Assess the morphology of the erythrocytes.
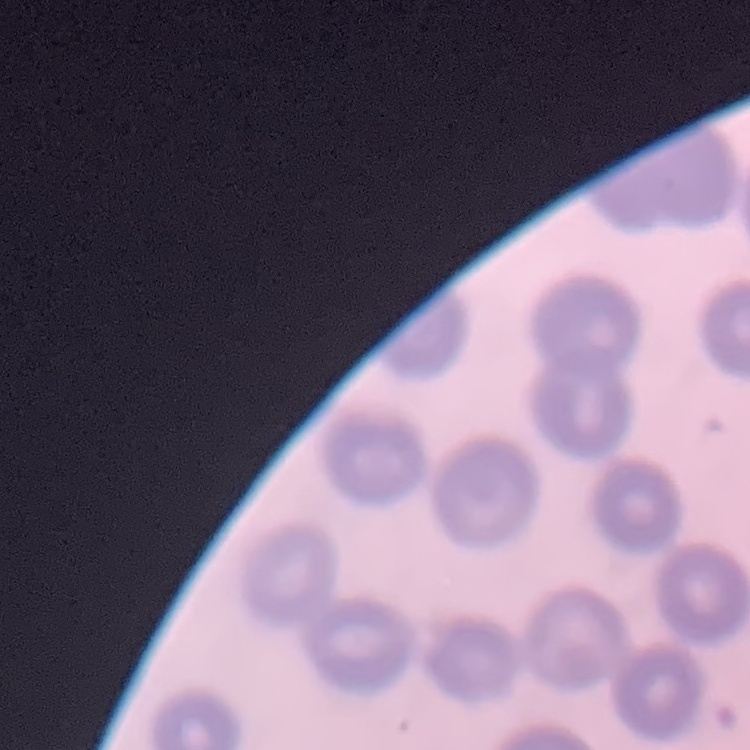
They show no rouleaux formation.

Field's or Giemsa stain. Thin blood film. One tile cut from a larger photomicrograph.